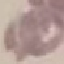
Summary:
  - Malaria status: uninfected
  - Image type: cell patch, automatically extracted from a larger field of view and resized to 64 × 64 pixels
  - Preparation: thin smear
  - Capture: smartphone camera at the microscope eyepiece
  - Stain: Giemsa